Assess this cell for malaria.
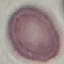
Uninfected.

Photographed with a smartphone camera at the microscope eyepiece. Giemsa-stained preparation. Thin smear of blood. Automatically extracted cell patch, resized to 64 × 64 pixels.